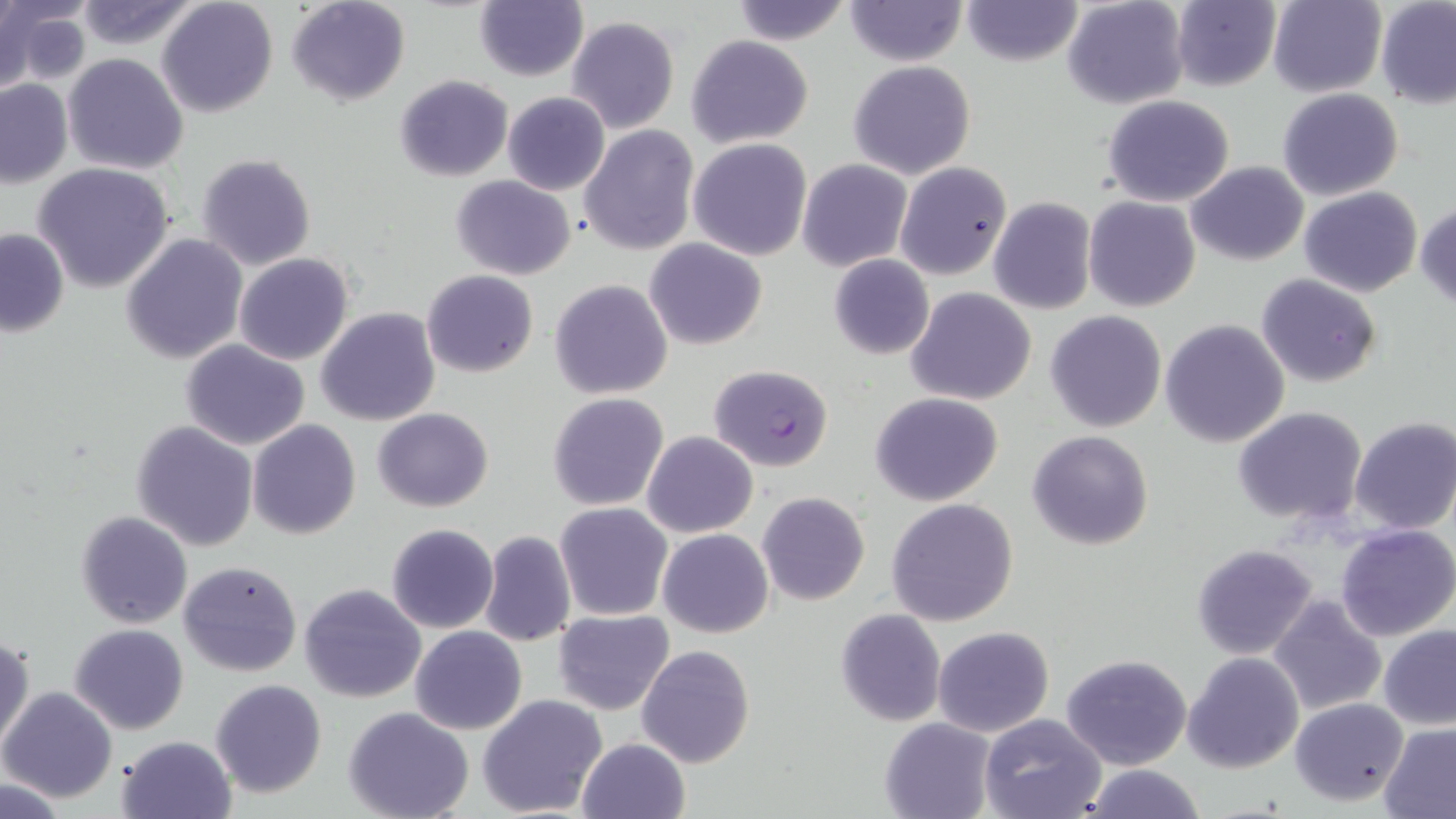

slide_level_diagnosis: Plasmodium falciparum
image_size: 1456×819 pixels
modality: optical microscopy
stain: May-Grünwald-Giemsa
uninfected_red_blood_cell_locations: 'approximate bounding boxes as [x1, y1, x2, y2] in pixels: [286, 0, 410, 106], [843, 0, 967, 67], [959, 0, 1084, 67], [1062, 0, 1189, 109], [1171, 0, 1283, 90], [1267, 0, 1386, 97], [72, 1, 198, 50], [157, 1, 277, 118], [727, 1, 855, 46], [1376, 1, 1456, 107], [0, 2, 89, 89], [474, 2, 588, 81], [566, 16, 681, 136], [686, 35, 814, 148], [62, 54, 188, 174], [848, 60, 976, 179], [394, 75, 513, 182], [0, 79, 73, 187], [1277, 87, 1405, 201], [503, 91, 611, 194], [1102, 94, 1236, 207], [579, 125, 699, 255], [688, 137, 814, 260], [196, 154, 317, 273], [796, 158, 913, 272], [895, 161, 1012, 280], [31, 162, 175, 293], [1186, 162, 1308, 266], [451, 174, 576, 280], [1298, 187, 1422, 296], [1280, 188, 1403, 384], [1084, 196, 1200, 312], [988, 197, 1096, 315], [1416, 202, 1456, 310], [0, 228, 70, 337], [120, 233, 248, 365], [645, 238, 766, 350], [233, 253, 354, 366], [829, 254, 934, 360], [262, 268, 418, 398], [422, 270, 538, 377], [1256, 273, 1383, 387], [550, 279, 674, 401], [907, 287, 1036, 405], [317, 307, 440, 426], [1044, 310, 1167, 432], [1160, 319, 1290, 448], [180, 339, 311, 452], [546, 392, 670, 511], [870, 392, 1004, 507], [1232, 406, 1369, 528], [372, 408, 494, 511], [1349, 417, 1456, 534], [247, 419, 361, 539], [130, 420, 259, 552], [1027, 430, 1154, 550], [642, 431, 759, 538], [757, 491, 870, 606], [886, 497, 1020, 627], [555, 503, 672, 621], [75, 510, 193, 628], [386, 524, 498, 633], [1337, 525, 1455, 642], [658, 528, 773, 639], [479, 529, 576, 648], [1192, 543, 1318, 660], [179, 560, 303, 678], [299, 583, 426, 703], [1268, 593, 1386, 715], [552, 609, 673, 714], [835, 609, 946, 726], [69, 623, 191, 735], [1378, 624, 1456, 729], [410, 625, 527, 734], [932, 626, 1054, 736], [0, 632, 33, 751], [636, 644, 756, 768], [19, 648, 138, 776], [1183, 651, 1304, 773], [1061, 654, 1193, 771], [210, 679, 327, 798], [1, 685, 118, 803], [477, 694, 607, 818], [1289, 697, 1409, 806], [343, 707, 474, 819], [979, 712, 1106, 819], [879, 718, 998, 819], [1380, 723, 1456, 817], [115, 734, 238, 819], [576, 737, 691, 819], [1079, 763, 1208, 819], [0, 777, 70, 817]'
magnification: 1000x
plasmodium_falciparum_infected_red_blood_cell_locations: 'approximate bounding boxes as [x1, y1, x2, y2] in pixels: [707, 364, 835, 471]'
preparation: thin blood film
field_of_view: single